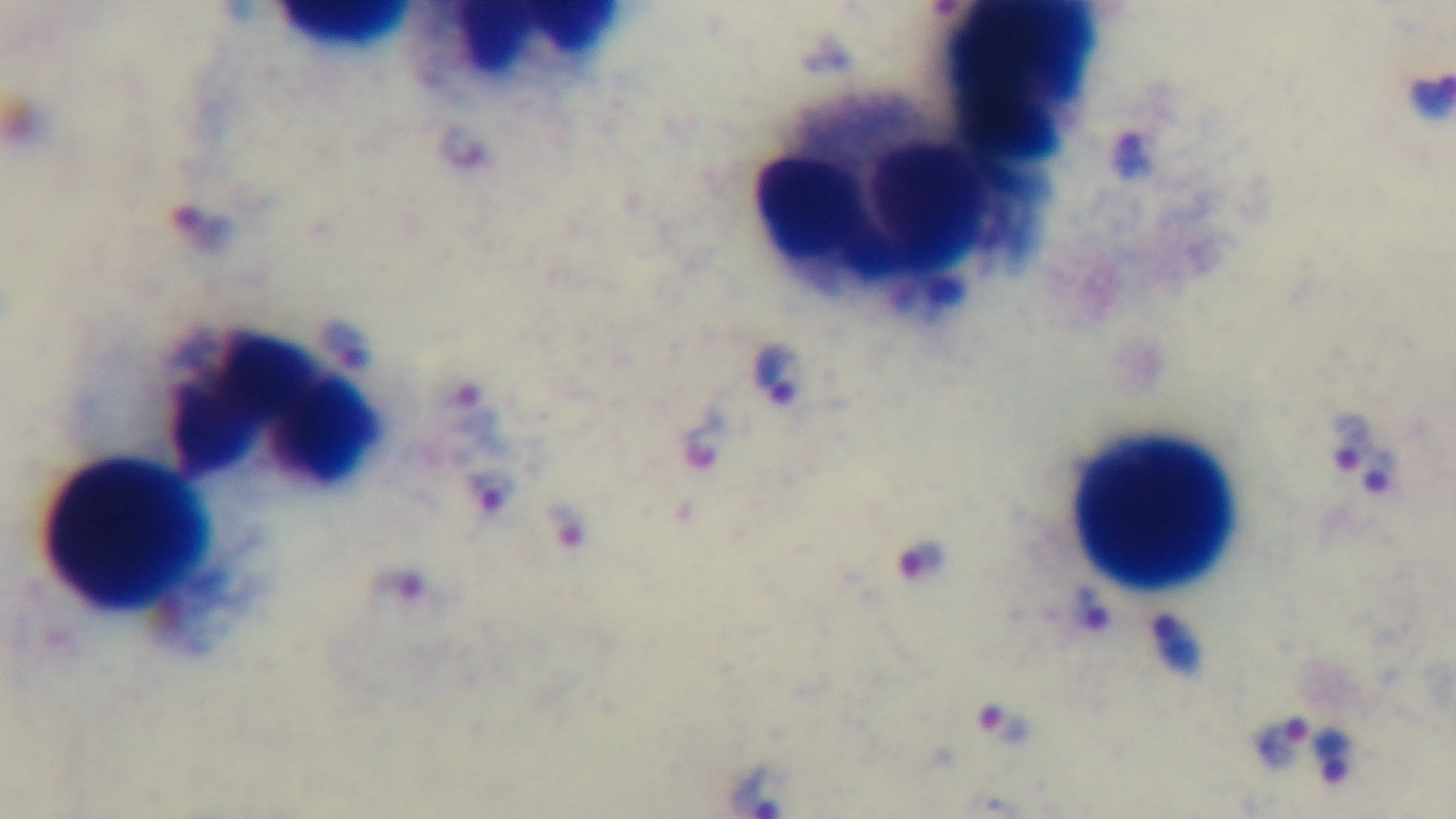

stain = Giemsa
objective = 100x oil immersion
field of view = one from the slide
modality = light microscopy
malaria status = infected
capture = mounted 4K digital camera
preparation = thick smear